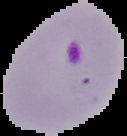

preparation = thin blood smear
image size = 127×136 pixels
malaria status = parasitized
image type = segmented cell region with the area outside set to black